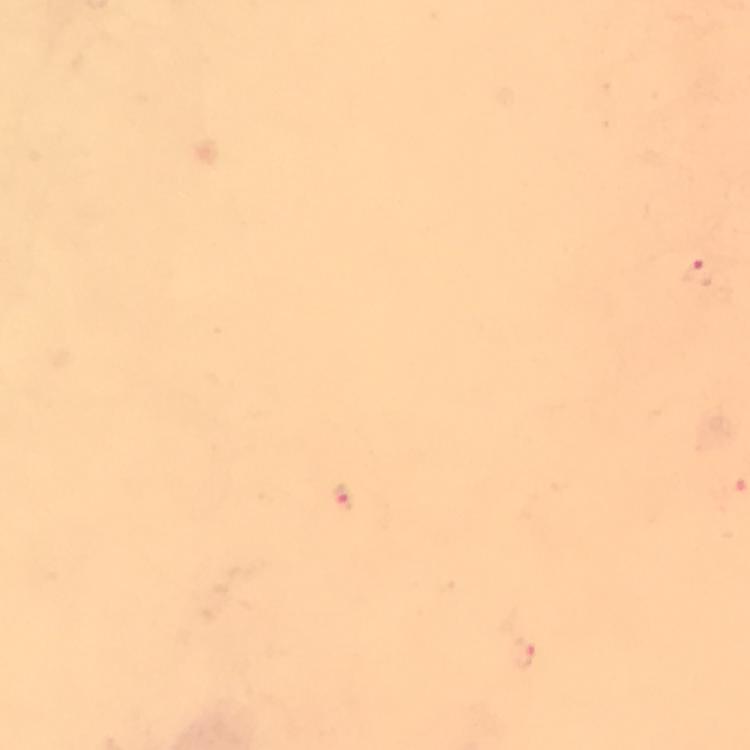 Approximate object centers, in pixels from the top-left corner. Malaria parasite locations: (x=697, y=273), (x=342, y=495). Image is 750×750 pixels. Photographed through the microscope with a smartphone camera. At 100x magnification. Giemsa-stained preparation. Thick smear. A crop from one field of view. From a diagnostic examination for malaria. Immersion oil applied.